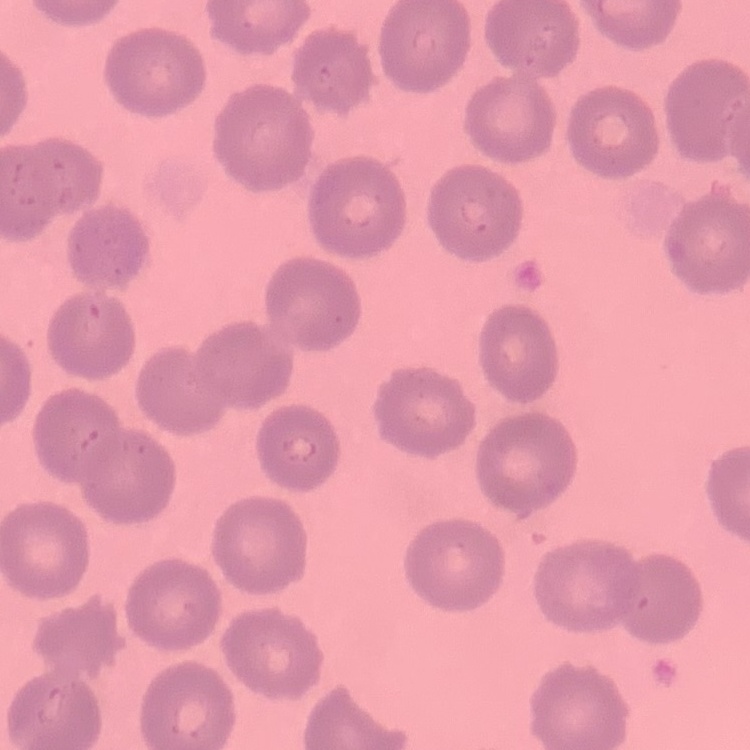
erythrocyte morphology = no rouleaux formation
preparation = thin peripheral smear
stain = Field's or Giemsa
image type = square crop of a larger photomicrograph